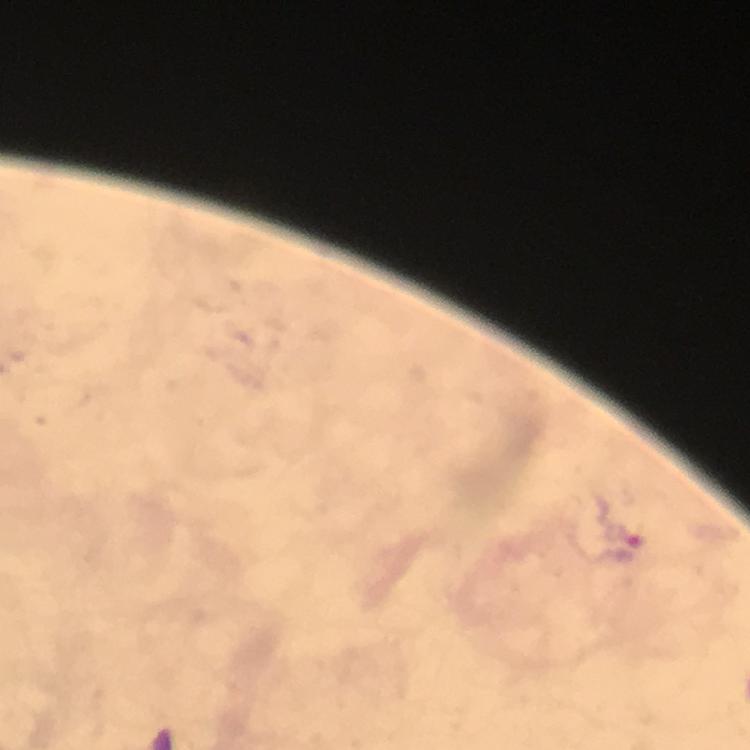
{
  "malaria_parasite_locations": "approximate object centers, in pixels from the top-left corner: (x=621, y=523)",
  "cropped_from": "one field of view",
  "context": "from a diagnostic examination for malaria",
  "image_size": "750×750 pixels",
  "stain": "Giemsa",
  "immersion_oil": "applied",
  "capture": "smartphone mounted on the microscope",
  "preparation": "thick smear",
  "magnification": "100x"
}